Report the malaria status of this cell.
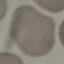
It is uninfected.

Summary:
  - Image type: cell patch, automatically extracted from a larger field of view and resized to 64 × 64 pixels
  - Capture: smartphone through the microscope eyepiece
  - Stain: Giemsa
  - Preparation: thin blood film